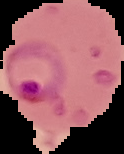
result = malaria parasites identified
preparation = thin blood smear
image type = segmented cell region on a black background
image size = 124×154 pixels